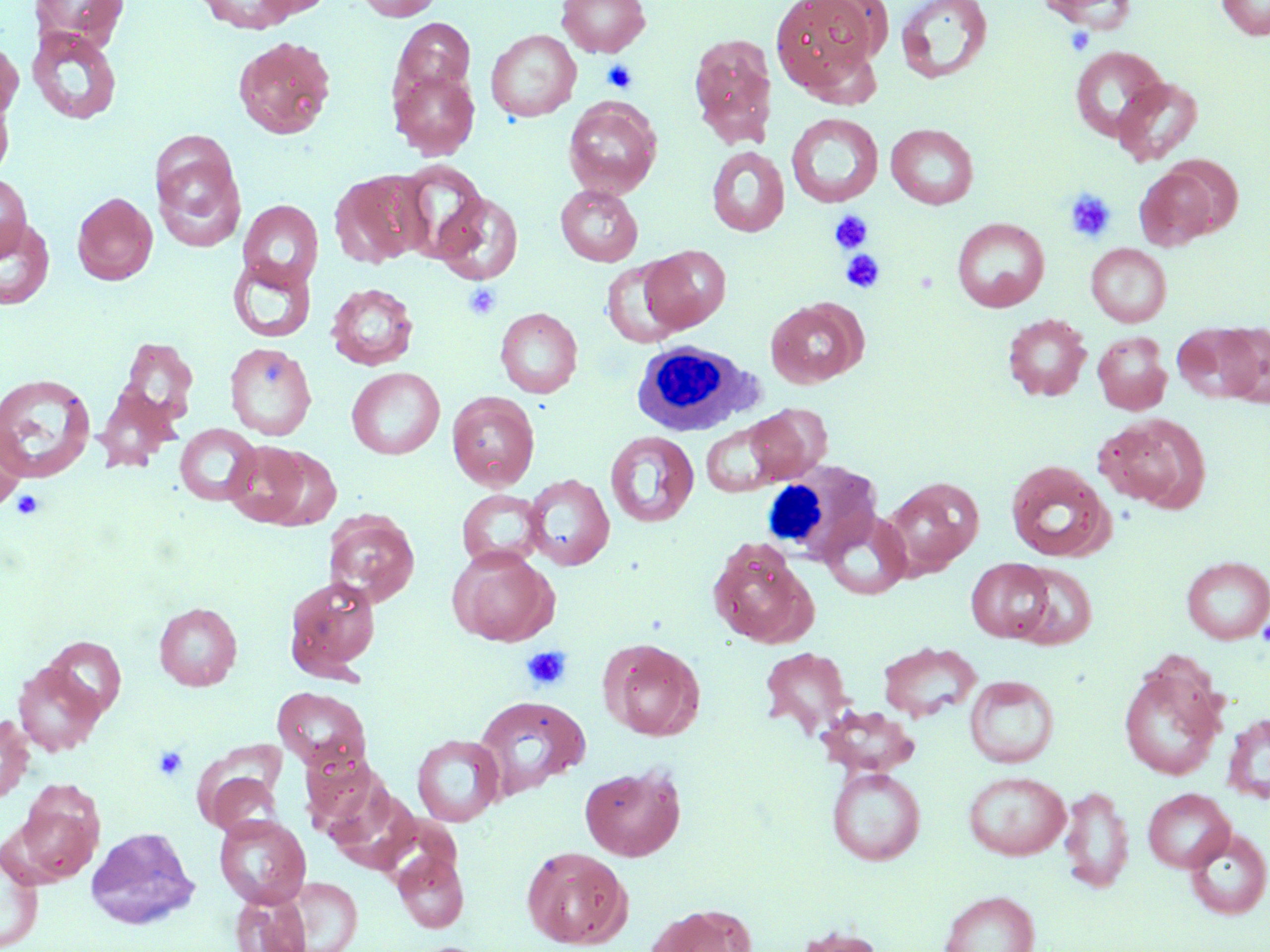

{
  "slide_level_diagnosis": "no evidence of blood parasites",
  "white_blood_cell_locations": "approximate bounding boxes as (x1,y1)-(x2,y2) corner pairs in pixels: (631,340)-(766,438), (761,458)-(882,567)",
  "image_size": "1270×952 pixels",
  "stain": "May-Grünwald-Giemsa",
  "modality": "light microscopy",
  "uninfected_red_blood_cell_locations": "approximate bounding boxes as (x1,y1)-(x2,y2) corner pairs in pixels: (30,0)-(130,48), (196,0)-(299,33), (253,0)-(334,18), (356,0)-(442,21), (557,0)-(651,58), (770,0)-(883,94), (895,0)-(993,84), (1033,0)-(1139,30), (1216,1)-(1270,40), (391,18)-(476,99), (26,27)-(123,125), (486,29)-(581,122), (689,34)-(778,148), (232,36)-(337,140), (0,39)-(23,122), (1069,45)-(1168,142), (389,68)-(480,159), (1113,76)-(1204,166), (0,90)-(15,181), (563,98)-(662,198), (786,113)-(884,208), (886,123)-(979,209), (149,137)-(247,252), (706,146)-(790,237), (393,162)-(488,262), (1133,166)-(1223,250), (330,170)-(432,268), (0,173)-(32,260), (555,184)-(643,266), (72,191)-(158,285), (432,192)-(523,284), (238,199)-(323,289), (0,217)-(55,310), (952,217)-(1050,312), (1086,243)-(1171,327), (640,245)-(730,333), (228,257)-(316,343), (601,259)-(686,348), (326,282)-(419,370), (765,299)-(865,388), (495,307)-(583,398), (1003,314)-(1091,401), (1173,323)-(1263,404), (1218,324)-(1270,409), (1092,331)-(1172,415), (119,337)-(200,427), (225,342)-(317,440), (346,367)-(445,460), (0,373)-(97,485), (93,383)-(179,472), (447,392)-(540,491), (743,404)-(831,485), (1096,413)-(1210,512), (700,420)-(794,496), (0,423)-(26,514), (174,423)-(262,506), (605,431)-(699,528), (223,441)-(315,528), (1005,460)-(1115,562), (523,473)-(615,570), (884,477)-(983,576), (456,489)-(547,570), (818,509)-(914,600), (323,511)-(420,607), (707,538)-(816,647), (447,547)-(559,646), (1181,556)-(1270,644), (966,558)-(1054,642), (1012,562)-(1097,649), (283,574)-(381,681), (154,602)-(241,691), (42,636)-(126,719), (600,639)-(703,741), (878,641)-(981,721), (759,646)-(856,738), (1118,660)-(1225,781), (14,662)-(104,755), (964,675)-(1059,768), (272,687)-(371,772), (473,695)-(590,799), (818,706)-(919,777), (1222,711)-(1270,805), (0,714)-(34,803), (412,734)-(505,827), (580,764)-(686,861), (827,766)-(925,865), (202,768)-(283,839), (962,771)-(1071,859), (12,784)-(104,885), (1059,784)-(1134,894), (1143,788)-(1234,872), (213,813)-(311,908), (86,826)-(199,929), (1184,828)-(1270,919), (521,846)-(632,948), (0,847)-(43,952), (391,849)-(469,933), (285,877)-(362,951), (939,890)-(1040,952), (230,892)-(310,952), (648,904)-(755,952), (791,925)-(885,952)",
  "platelet_locations": "approximate bounding boxes as (x1,y1)-(x2,y2) corner pairs in pixels: (1064,25)-(1097,56), (601,58)-(639,93), (1064,189)-(1117,242), (829,210)-(873,253), (841,249)-(887,293), (463,282)-(503,321), (11,489)-(46,520), (521,645)-(573,692), (153,745)-(188,781)",
  "magnification": "1000x",
  "field_of_view": "one of a larger specimen",
  "preparation": "thin blood smear"
}